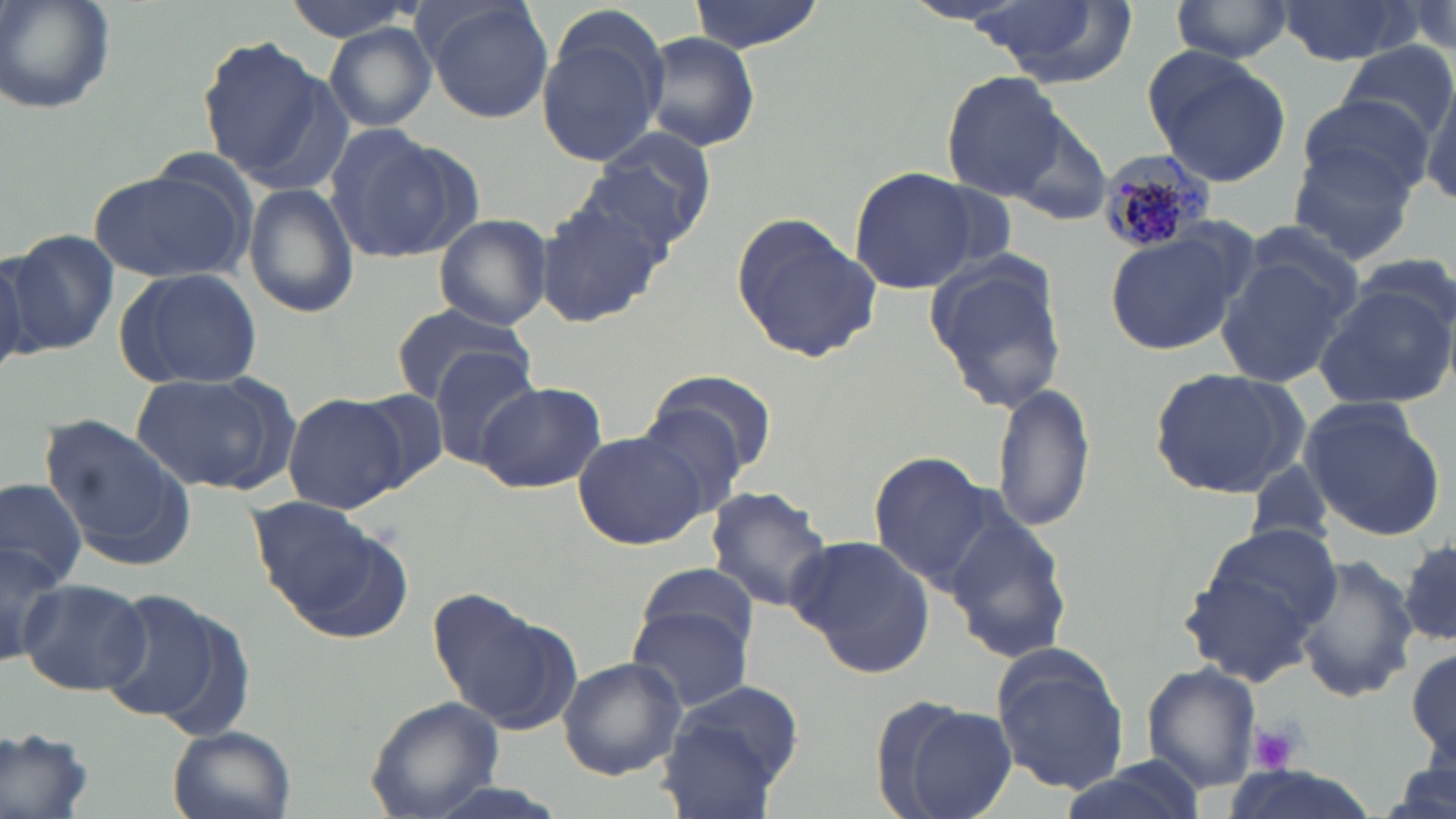

Approximate bounding boxes as (x1,y1)-(x2,y2) corner pairs in pixels. White blood cell locations: (1,728)-(99,819). Uninfected red blood cell locations: (0,0)-(119,115), (278,0)-(419,44), (421,0)-(555,123), (687,0)-(822,53), (959,0)-(1127,81), (1167,0)-(1295,66), (1275,0)-(1421,66), (534,12)-(669,169), (322,20)-(438,131), (639,32)-(761,153), (197,35)-(338,189), (1334,42)-(1455,148), (1146,48)-(1290,185), (942,70)-(1066,200), (1422,78)-(1456,208), (1298,93)-(1432,198), (1001,106)-(1118,230), (324,126)-(465,262), (586,129)-(720,254), (1287,137)-(1421,266), (848,166)-(984,293), (90,170)-(245,283), (242,182)-(360,320), (535,194)-(672,329), (730,211)-(881,363), (433,212)-(552,331), (1104,227)-(1247,357), (4,229)-(117,358), (1213,243)-(1358,388), (0,245)-(39,373), (922,251)-(1067,413), (1353,251)-(1454,345), (114,266)-(263,390), (1313,280)-(1455,411), (388,303)-(537,406), (430,349)-(543,463), (1147,367)-(1309,500), (642,369)-(774,497), (134,373)-(283,493), (477,381)-(607,494), (990,381)-(1095,535), (353,389)-(451,490), (284,394)-(406,513), (1301,400)-(1447,542), (38,414)-(197,572), (571,428)-(709,552), (868,452)-(998,585), (0,477)-(86,592), (705,485)-(836,613), (246,498)-(401,628), (942,512)-(1076,661), (0,532)-(68,663), (789,534)-(936,679), (1402,538)-(1456,646), (1182,546)-(1332,684), (1293,555)-(1420,702), (634,562)-(760,655), (18,577)-(152,694), (430,586)-(578,733), (97,588)-(220,720), (626,607)-(752,712), (989,645)-(1129,796), (1407,647)-(1456,760), (557,656)-(687,781), (1140,662)-(1261,793), (657,685)-(807,819), (363,696)-(507,819), (886,697)-(1017,819), (166,725)-(295,819), (0,730)-(102,819), (1389,757)-(1456,819). Plasmodium malariae-infected red blood cell locations: (1096,154)-(1218,255). Platelet locations: (1249,720)-(1301,775). Slide-level diagnosis: Plasmodium malariae. Thin blood film. Optical microscopy. May-Grünwald-Giemsa-stained preparation. Image is 1456×819 pixels. 1000x magnification. One field of a larger specimen.